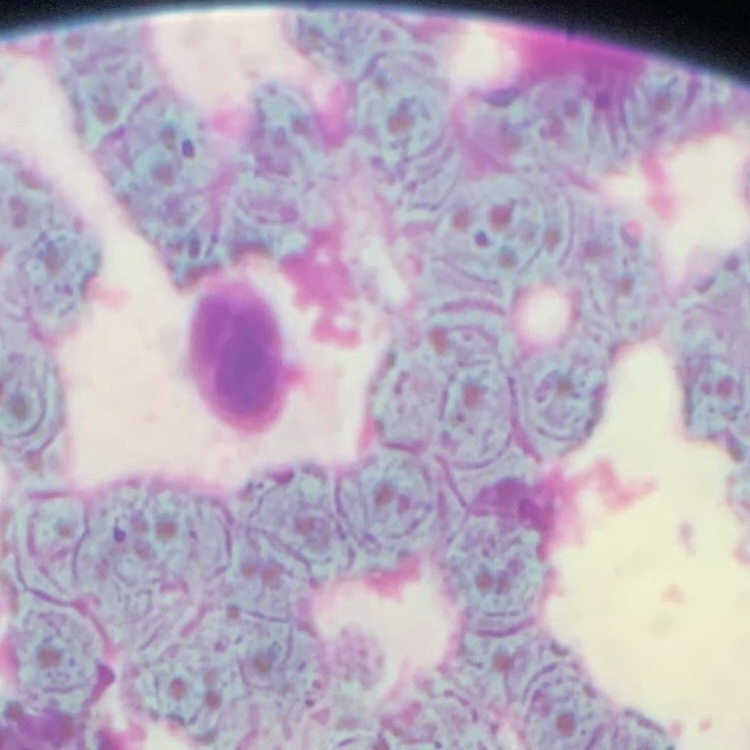 The red blood cells exhibit rouleaux formation. Thin blood smear. One tile cut from a larger photomicrograph. Stained with either Field's or Giemsa.